Evaluate for Plasmodium parasites.
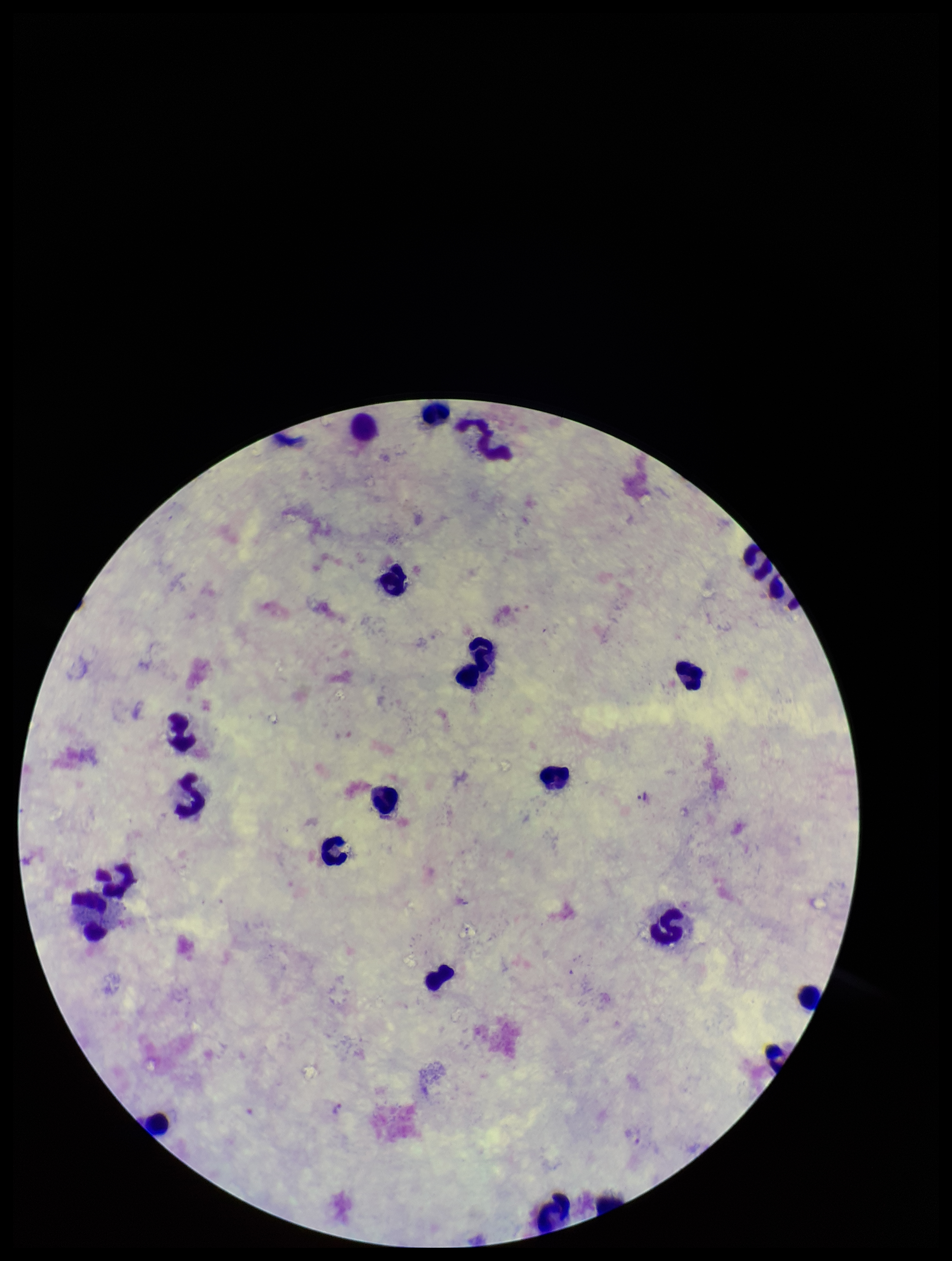
Identified.

image size = 952×1261 pixels
preparation = thick smear
capture = smartphone photograph through the microscope eyepiece
parasite count = 2
patient malaria status = infected
leukocyte count = 21
field of view = one from this slide
stain = Giemsa
species reported for this patient = Plasmodium vivax